Identify the blood parasite species.
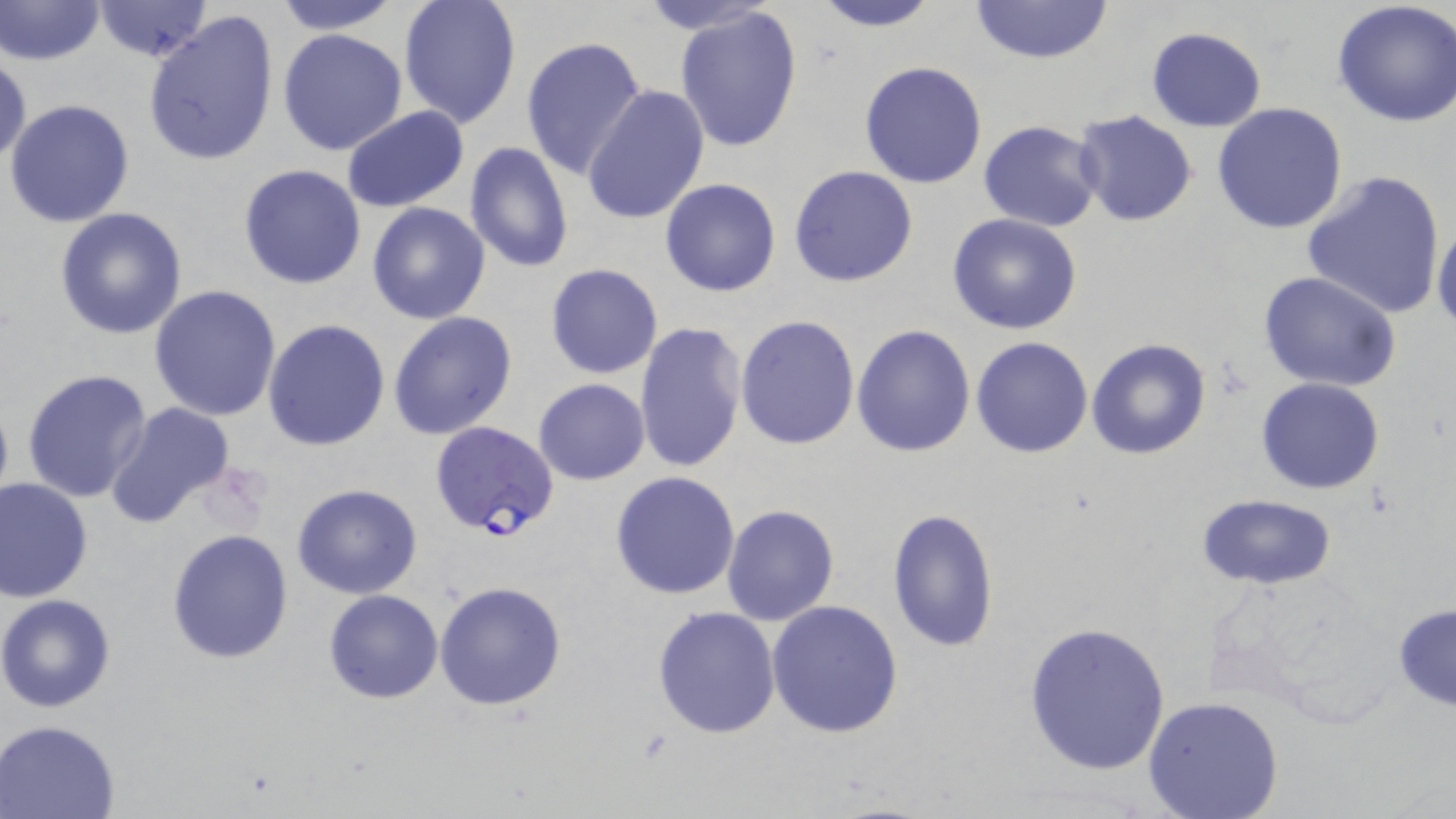
Plasmodium falciparum.

preparation: thin blood smear
plasmodium_falciparum_infected_red_blood_cell_locations: 'approximate bounding boxes as (x1,y1)-(x2,y2) corner pairs in pixels: (429,421)-(560,539)'
field_of_view: single
modality: optical microscopy
image_size: 1456×819 pixels
uninfected_red_blood_cell_locations: 'approximate bounding boxes as (x1,y1)-(x2,y2) corner pairs in pixels: (0,0)-(105,67), (269,0)-(406,34), (634,0)-(785,37), (809,0)-(942,31), (967,0)-(1114,65), (1333,0)-(1456,127), (398,1)-(522,128), (89,2)-(216,64), (673,6)-(804,153), (143,10)-(279,167), (1146,27)-(1266,130), (277,29)-(408,156), (521,36)-(649,183), (1,51)-(31,168), (858,60)-(988,189), (582,85)-(710,227), (4,99)-(135,229), (1211,103)-(1347,232), (340,106)-(472,213), (1075,110)-(1198,226), (978,121)-(1103,232), (464,141)-(573,272), (238,164)-(367,289), (788,164)-(918,287), (1301,168)-(1446,320), (660,178)-(783,297), (366,201)-(492,325), (56,207)-(187,340), (946,213)-(1083,335), (1433,217)-(1456,333), (544,262)-(663,380), (1258,270)-(1401,392), (148,284)-(282,422), (388,311)-(518,439), (734,313)-(860,451), (262,318)-(390,451), (632,321)-(747,477), (851,324)-(976,458), (971,337)-(1093,457), (1087,338)-(1213,460), (22,368)-(153,505), (1256,377)-(1386,494), (534,379)-(650,484), (106,403)-(236,528), (610,471)-(742,600), (1,479)-(94,603), (292,483)-(423,599), (1193,494)-(1338,589), (721,504)-(841,627), (885,507)-(999,655), (167,529)-(294,664), (434,580)-(568,710), (323,589)-(443,705), (1,593)-(118,713), (767,599)-(904,739), (1393,603)-(1456,710), (651,605)-(783,739), (1022,621)-(1172,774), (1142,697)-(1284,819), (1,719)-(121,818)'
magnification: 1000x
stain: May-Grünwald-Giemsa